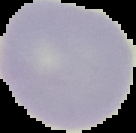

image type = segmented cell region with the area outside set to black
image size = 136×133 pixels
preparation = thin blood smear
result = no Plasmodium parasites detected